Comment on the morphology of the red blood cells.
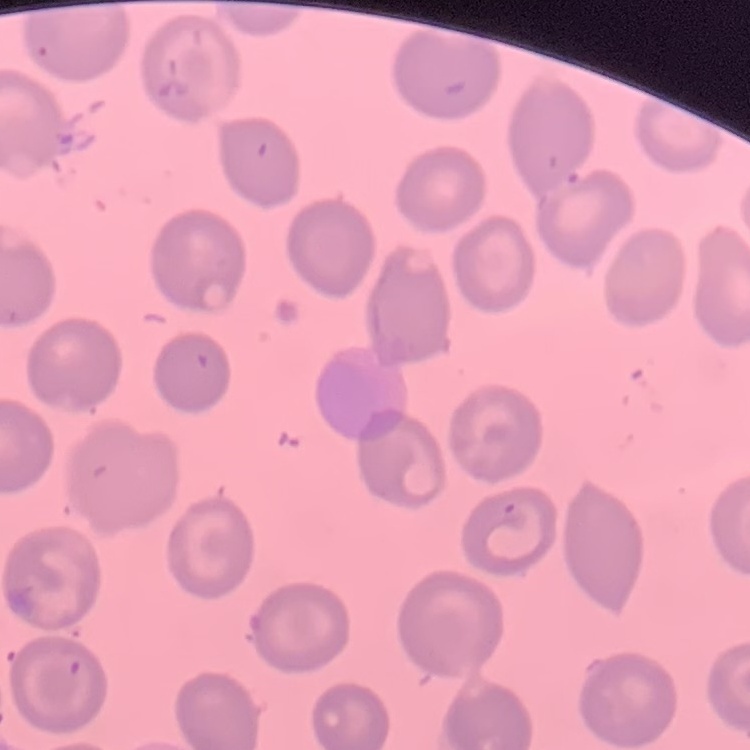
They show no rouleaux formation.

image type = one tile cut from a larger photomicrograph
preparation = thin peripheral smear
stain = Field's or Giemsa